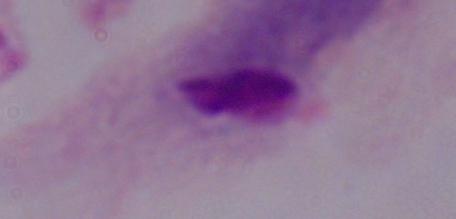
1000x magnification. Micrograph. A trichomonad is seen.